Report the malaria status of this cell.
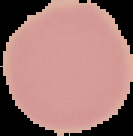
Uninfected.

Summary:
  - Image type: segmented cell region with the area outside set to black
  - Preparation: thin blood film
  - Image size: 133×136 pixels